Describe the morphology of the red blood cells.
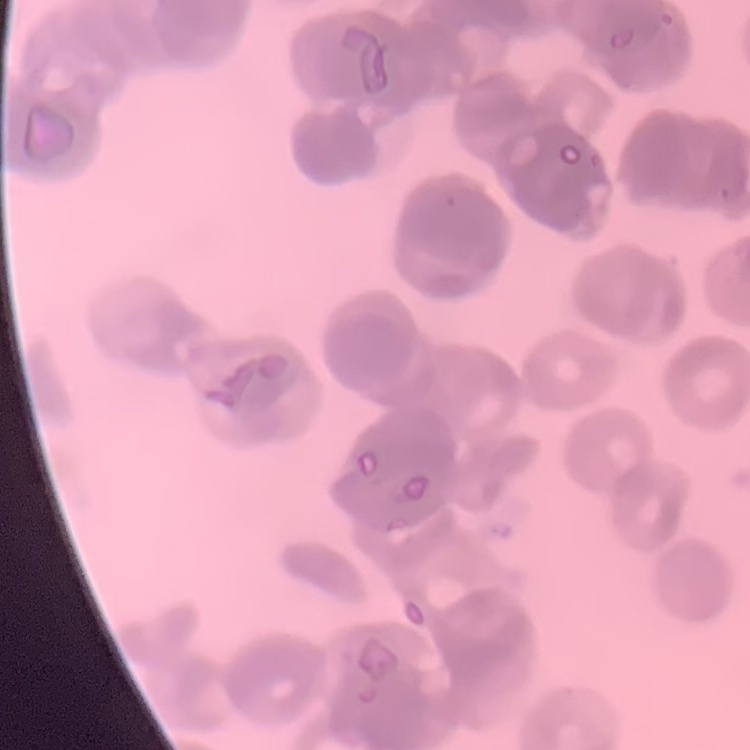
They show rouleaux formation.

image type = one tile cut from a larger photomicrograph
preparation = thin peripheral smear
stain = Field's or Giemsa